Classify this cell by malaria status.
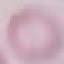

Uninfected.

preparation: thin blood smear
image_type: cell patch, automatically extracted from a larger field of view and resized to 64 × 64 pixels
capture: smartphone camera at the microscope eyepiece
stain: Giemsa